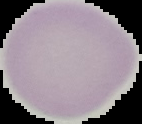

From a thin blood smear. Malaria status: uninfected. Segmented cell region on a black background. Image is 142×124 pixels.